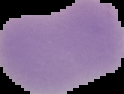

image type = segmented cell region with the area outside set to black
result = no Plasmodium parasites detected
image size = 124×94 pixels
preparation = thin blood film